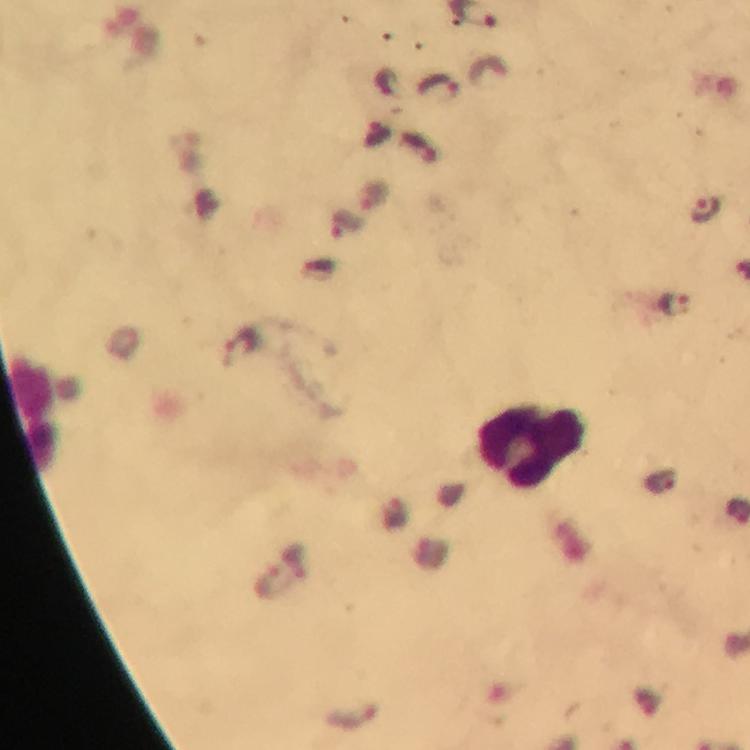 Approximate centers as {x, y} in pixels. Leukocyte locations: {530, 445}. Plasmodium parasite locations: {440, 87}, {378, 132}, {420, 148}, {704, 210}, {347, 226}, {675, 305}, {242, 346}, {659, 481}. Giemsa-stained preparation. Image is 750×750 pixels. Immersion oil applied. 100x magnification. A crop from one field of view. Smartphone photograph taken through a microscope. From a malaria diagnostic workup. Thick smear.